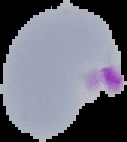

From a thin blood smear. Image is 127×142 pixels. Malaria status: parasitized. Segmented cell region on a black background.